Name the parasite shown.
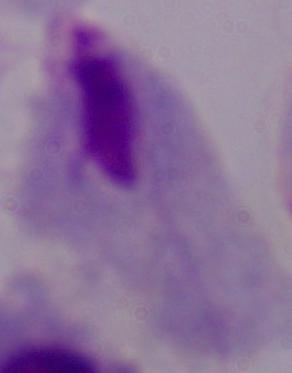

This is a trichomonad.

modality = micrograph
magnification = 1000x